Identify the cell.
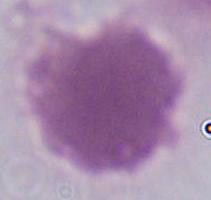
This is an erythrocyte.

Captured at 1000x magnification. Micrograph.